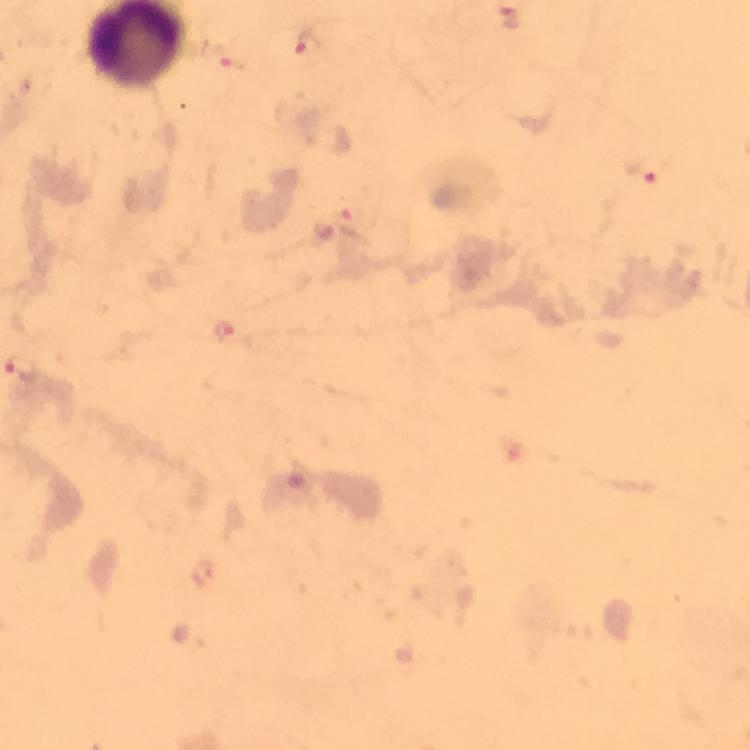

Approximate centers as [x, y] in pixels. Malaria parasite locations: [513, 19], [309, 46], [648, 170], [225, 331]. At 100x magnification. Giemsa stain. Cropped region of a single field of view. Immersion oil was used. Thick smear. Image is 750×750 pixels. From a diagnostic examination for malaria. Photographed with a smartphone mounted on the microscope.